Report the malaria status of this cell.
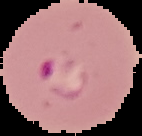

Parasitized.

image size = 142×136 pixels
preparation = thin blood film
image type = segmented cell region on a black background